Evaluate for Plasmodium parasites.
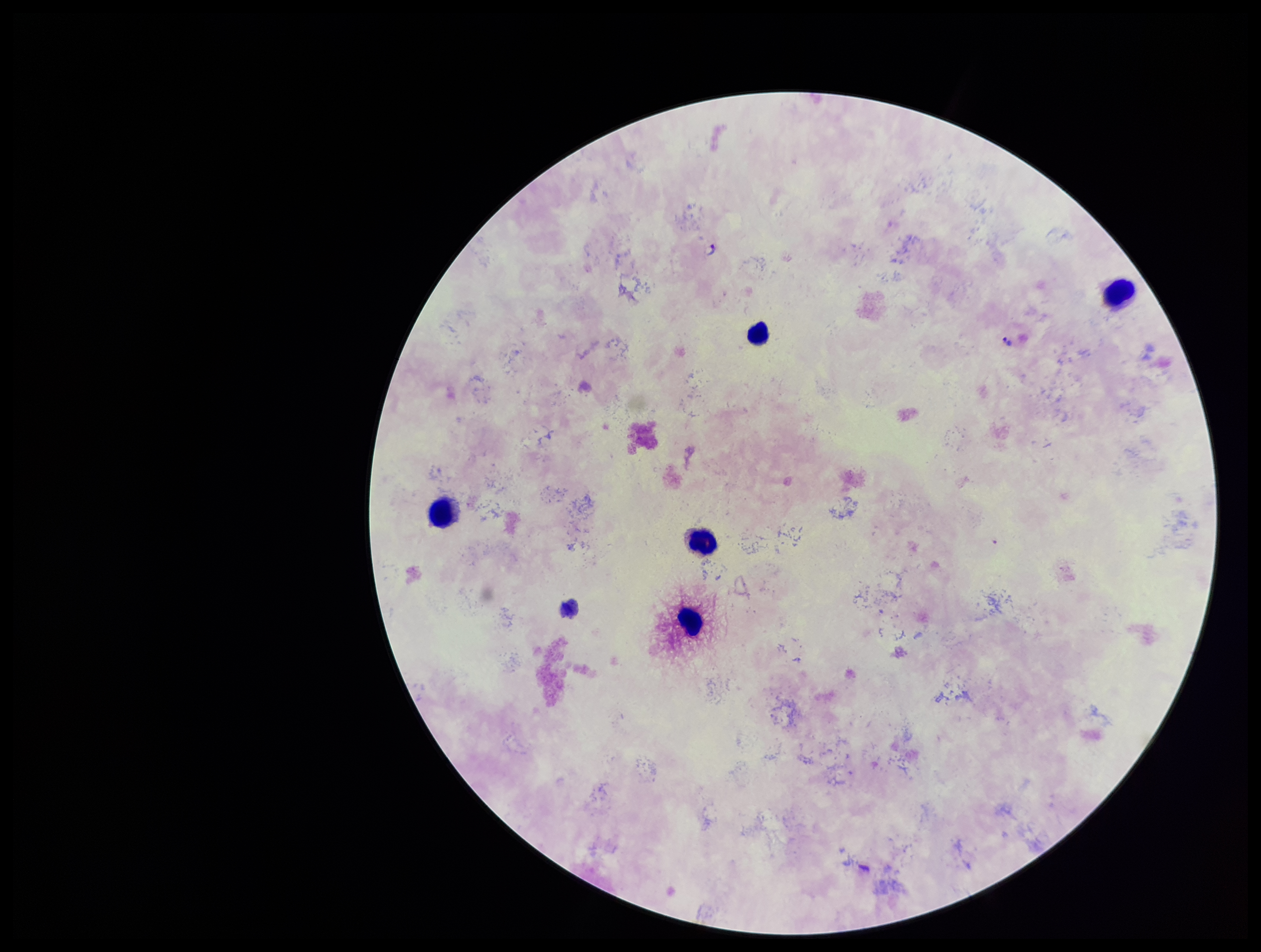
Seen.

stain = Giemsa
patient malaria status = infected
preparation = thick blood smear
field of view = one from this slide
capture = smartphone photograph through the microscope eyepiece
species reported for this patient = Plasmodium falciparum
leukocyte count = 5
image size = 1261×952 pixels
parasite count = 2